Outline each blood parasite and name the species.
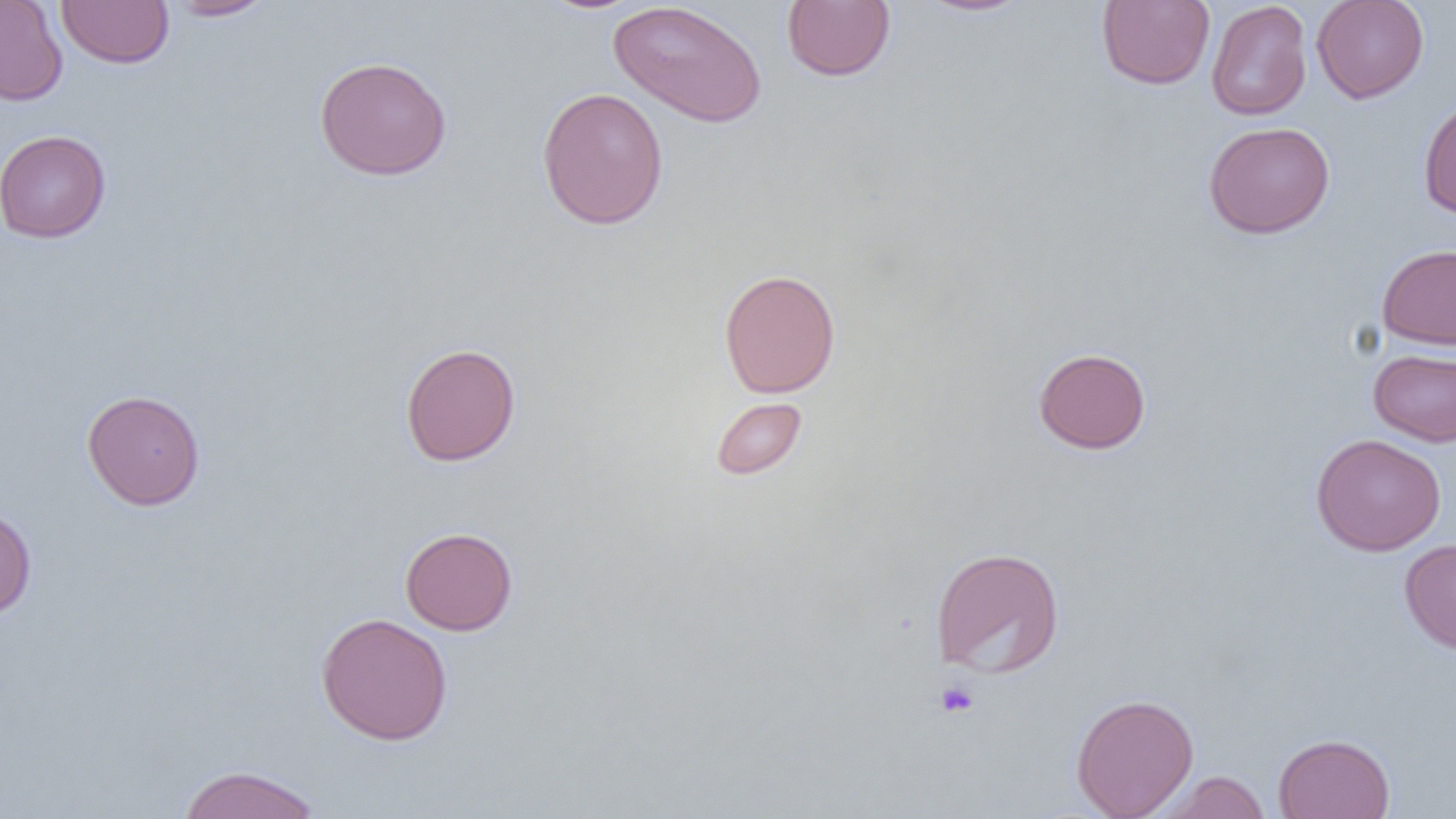

No blood parasites seen.

Summary:
  - Coordinate format: approximate bounding boxes as named x1/y1/x2/y2 corners in pixels
  - Platelet locations: (x1=934, y1=680, x2=979, y2=718)
  - Uninfected red blood cell locations: (x1=0, y1=0, x2=68, y2=106), (x1=56, y1=0, x2=174, y2=68), (x1=164, y1=0, x2=278, y2=21), (x1=781, y1=0, x2=895, y2=81), (x1=915, y1=0, x2=1034, y2=17), (x1=1096, y1=0, x2=1215, y2=90), (x1=1311, y1=0, x2=1429, y2=103), (x1=608, y1=1, x2=768, y2=129), (x1=1206, y1=1, x2=1312, y2=121), (x1=314, y1=55, x2=452, y2=181), (x1=536, y1=86, x2=669, y2=230), (x1=1418, y1=95, x2=1456, y2=218), (x1=1203, y1=121, x2=1335, y2=239), (x1=0, y1=129, x2=111, y2=243), (x1=1377, y1=244, x2=1456, y2=350), (x1=719, y1=268, x2=840, y2=399), (x1=400, y1=342, x2=521, y2=467), (x1=1033, y1=347, x2=1151, y2=454), (x1=1368, y1=348, x2=1456, y2=447), (x1=82, y1=389, x2=205, y2=510), (x1=711, y1=397, x2=808, y2=480), (x1=1310, y1=433, x2=1447, y2=556), (x1=0, y1=506, x2=37, y2=620), (x1=399, y1=526, x2=519, y2=635), (x1=1399, y1=538, x2=1456, y2=655), (x1=930, y1=546, x2=1065, y2=679), (x1=316, y1=612, x2=453, y2=745), (x1=1071, y1=693, x2=1199, y2=818), (x1=1273, y1=733, x2=1395, y2=819), (x1=176, y1=764, x2=323, y2=819), (x1=1154, y1=771, x2=1271, y2=819)
  - Slide-level diagnosis: negative for blood parasites
  - Magnification: 1000x
  - Preparation: thin blood smear
  - Image size: 1456×819 pixels
  - Modality: light microscopy
  - Field of view: one of a larger specimen